Give the position of every leukocyte visible.
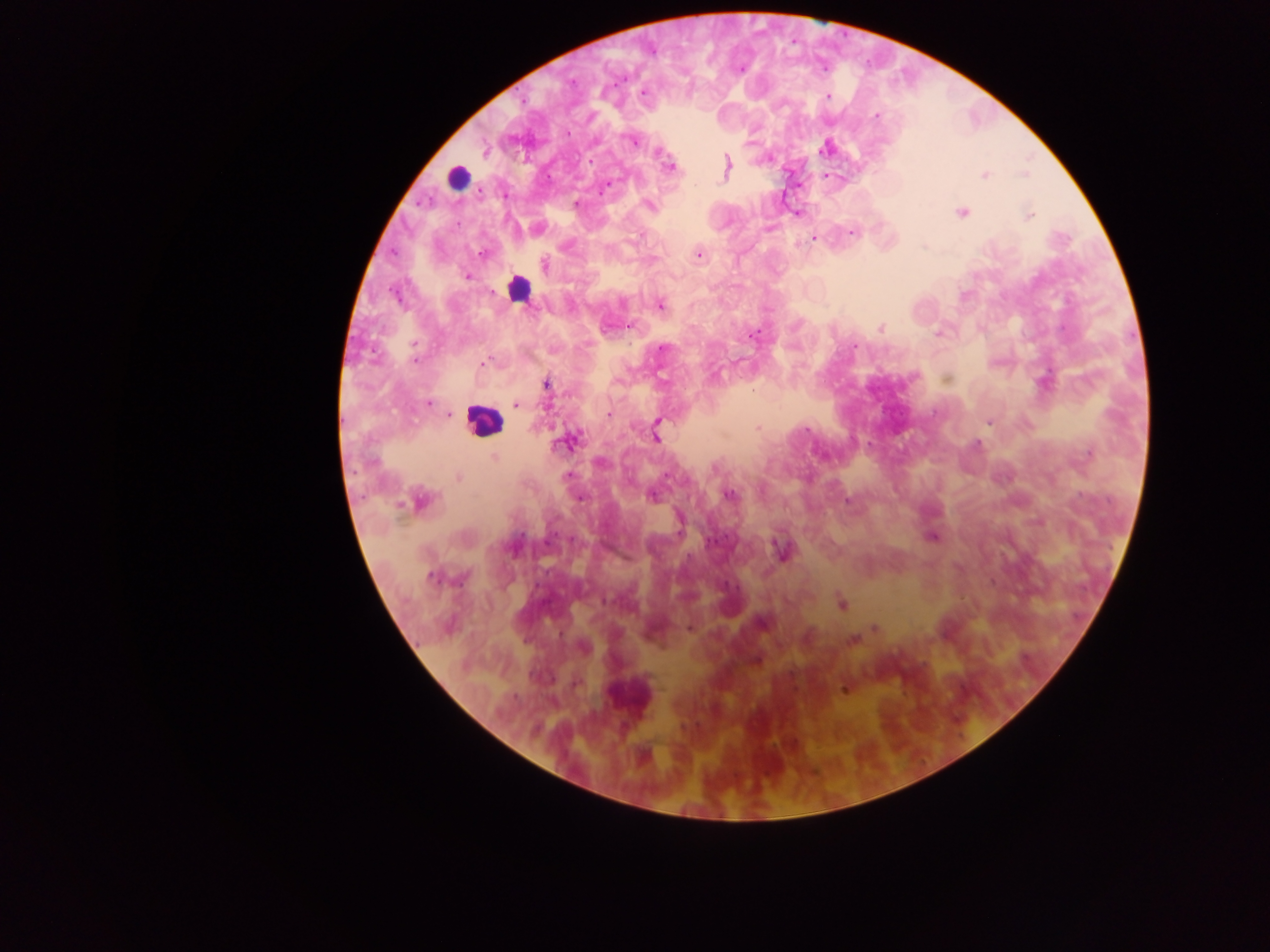
Approximate centers as {x, y} in pixels.
Leukocytes: {456, 178}, {518, 288}, {483, 420}.

Plasmodium parasite locations = approximate centers as {x, y} in pixels: {573, 82}, {643, 94}, {827, 96}, {877, 116}, {632, 141}, {825, 149}, {659, 153}, {670, 165}, {726, 167}, {985, 175}, {604, 187}, {505, 194}, {576, 204}, {649, 206}, {962, 212}, {1030, 215}, {851, 232}, {813, 239}, {481, 254}, {699, 255}, {545, 265}, {467, 277}, {396, 297}, {661, 305}, {629, 326}, {880, 328}, {937, 333}, {754, 334}, {854, 346}, {663, 348}, {414, 361}, {484, 363}, {547, 385}, {429, 403}, {516, 405}, {449, 414}, {609, 414}, {657, 422}, {989, 422}, {757, 428}, {806, 430}, {656, 437}, {570, 441}, {977, 445}, {1089, 453}, {494, 458}, {567, 476}, {458, 477}, {729, 495}, {652, 497}, {578, 498}, {847, 500}, {420, 501}, {932, 538}, {782, 551}, {432, 578}, {462, 578}, {842, 604}, {762, 622}, {690, 628}, {875, 628}, {852, 640}, {584, 648}, {756, 660}, {843, 690}
preparation = thick blood film
capture = mobile-phone photograph through a microscope
field of view = single
image size = 1270×952 pixels
country = Ghana